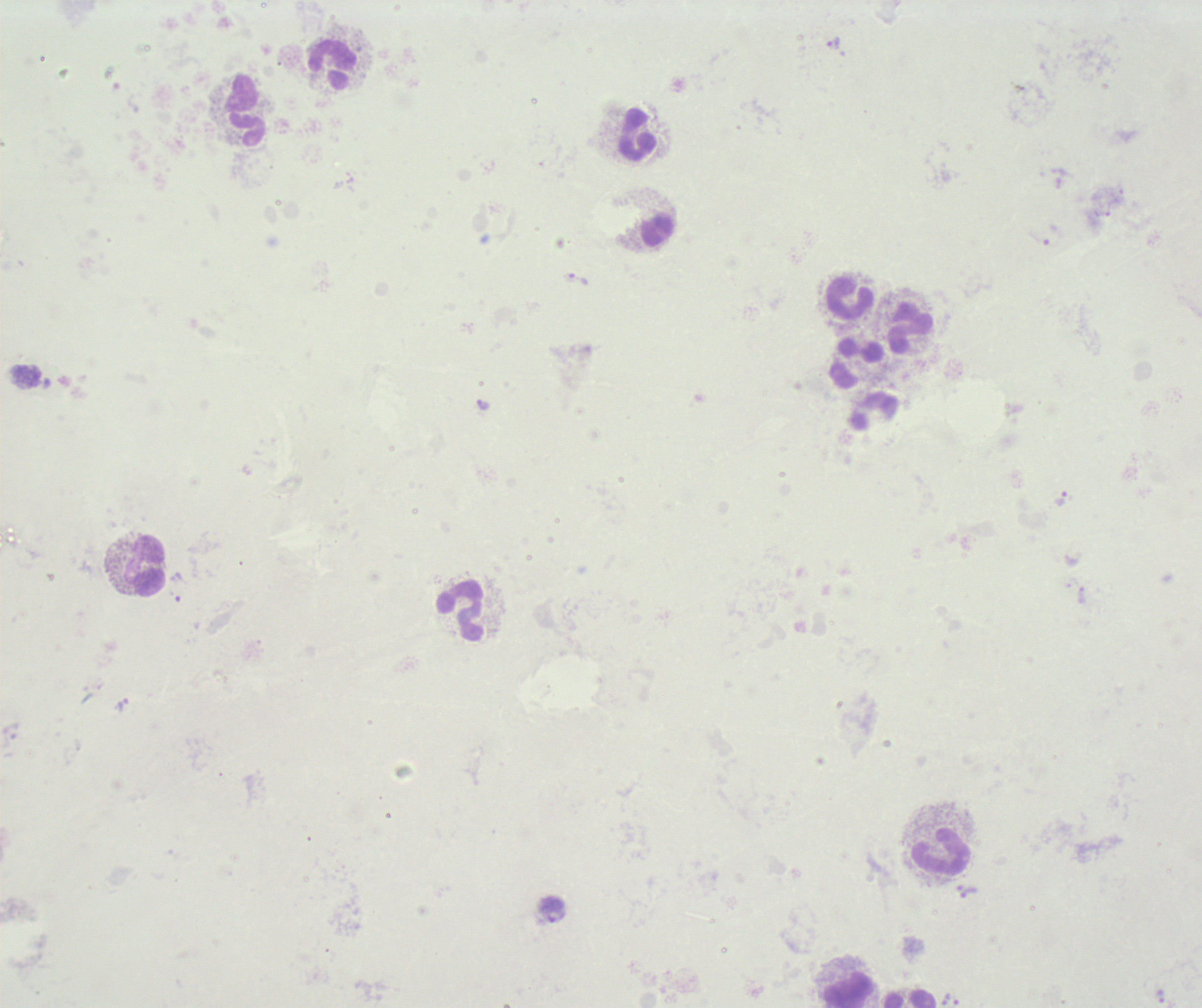
Approximate centers as (x, y) in pixels. Trophozoite locations: (833, 44), (579, 280), (483, 404), (1061, 499), (123, 704), (968, 892), (1159, 996), (950, 1003). Leukocyte locations: (331, 67), (244, 110), (636, 134), (655, 229), (850, 300), (910, 327), (855, 361), (873, 410), (146, 565), (462, 611), (940, 853), (849, 988), (909, 998). Previously used in a real diagnosis. Thick blood film. Result: positive for Plasmodium parasites. Image is 1202×1008 pixels. 100x magnification. Romanowsky stain. Single field of view. Background quality: unsatisfactory.